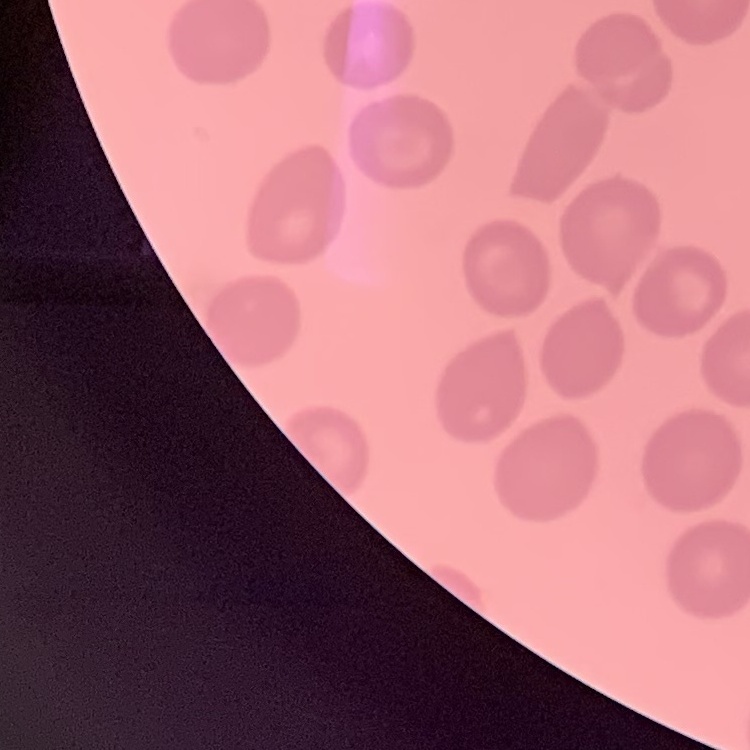

erythrocyte morphology = no rouleaux formation
stain = Field's or Giemsa
image type = square crop of a larger photomicrograph
preparation = thin peripheral smear